State which parasite is depicted.
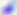
This is Toxoplasma gondii.

Micrograph. 400x magnification.